Assess this cell for malaria.
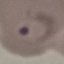

Parasitized.

Thin blood film. Automatically extracted cell patch, resized to 64 × 64 pixels. Giemsa stain. Acquired by smartphone through the microscope eyepiece.